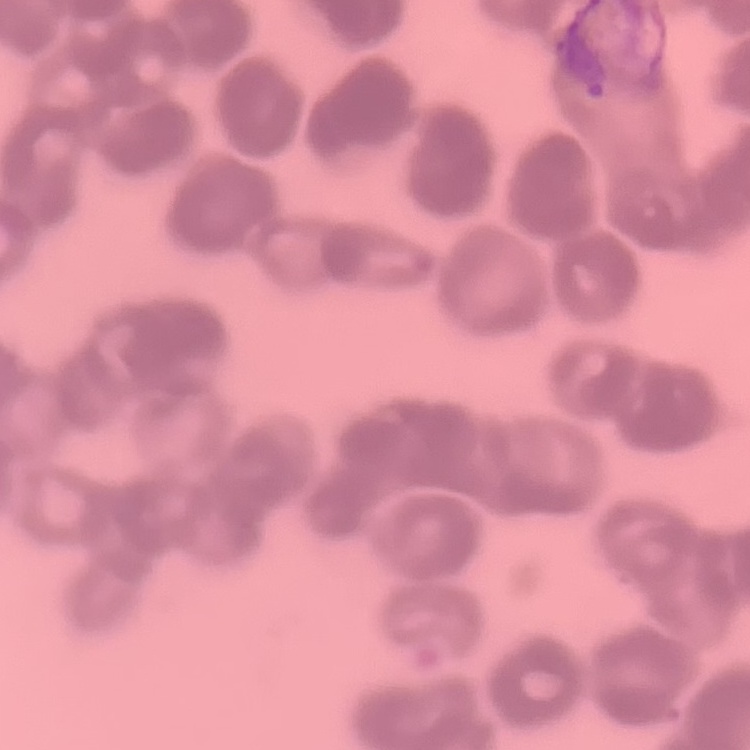

Summary:
  - Red blood cell morphology: rouleaux formation
  - Preparation: thin blood film
  - Stain: Field's or Giemsa
  - Image type: one tile cut from a larger photomicrograph